Locate every uninfected red blood cell.
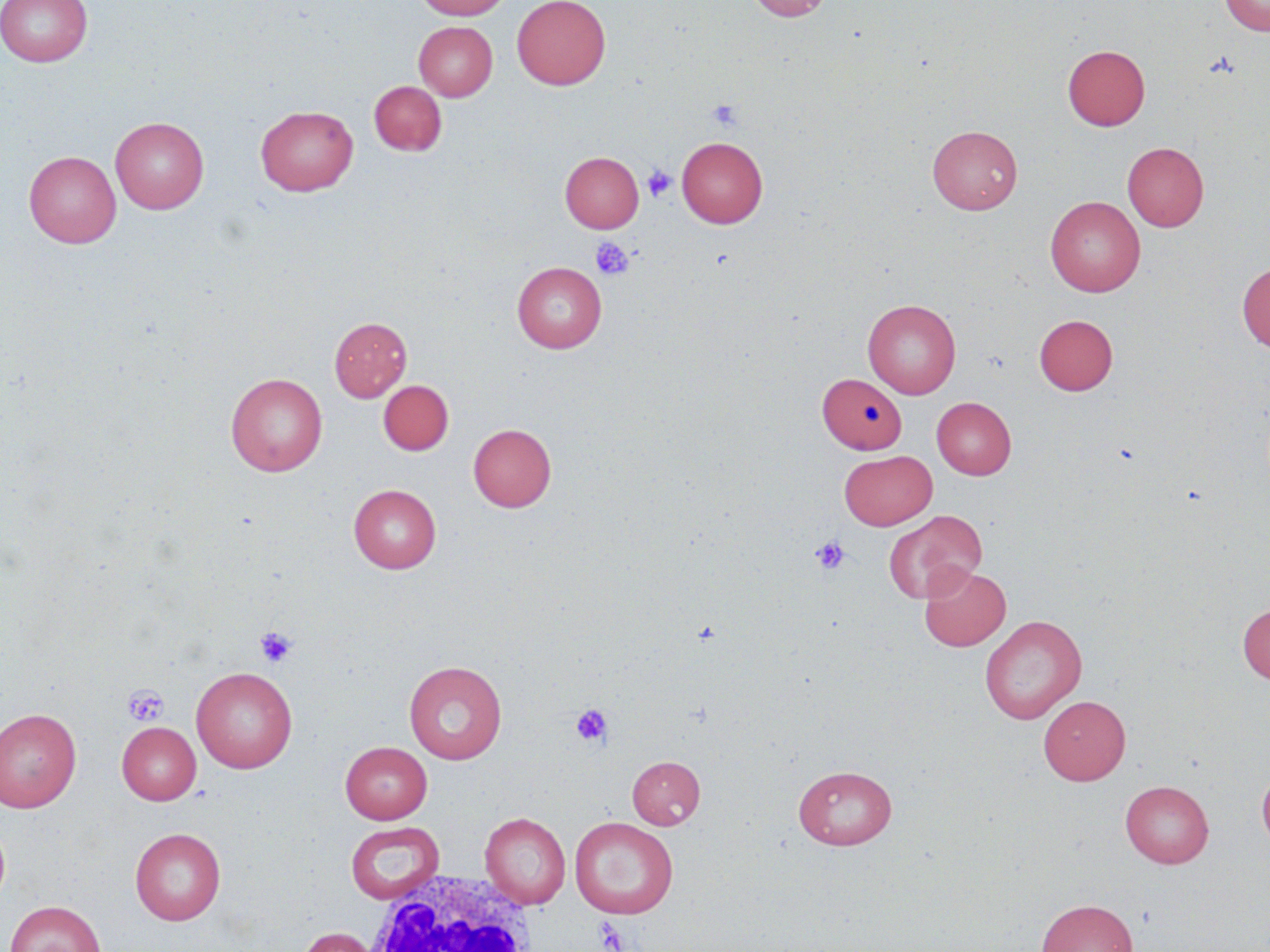

Approximate bounding boxes as [x1, y1, x2, y2] in pixels.
Uninfected red blood cells: [0, 0, 93, 66], [416, 0, 512, 19], [512, 0, 610, 90], [748, 0, 832, 21], [1219, 0, 1270, 36], [414, 21, 497, 101], [1063, 45, 1150, 130], [369, 80, 447, 156], [256, 105, 358, 196], [111, 116, 208, 213], [927, 125, 1022, 214], [677, 137, 767, 228], [1122, 142, 1208, 231], [24, 151, 121, 247], [560, 151, 644, 232], [1045, 196, 1145, 296], [512, 261, 606, 353], [1237, 262, 1270, 353], [863, 299, 961, 399], [1034, 314, 1118, 395], [330, 316, 412, 402], [818, 372, 906, 454], [226, 373, 328, 476], [378, 380, 454, 455], [932, 397, 1016, 479], [468, 423, 556, 512], [839, 450, 936, 530], [349, 484, 441, 573], [884, 509, 985, 603], [919, 564, 1011, 651], [1237, 603, 1270, 684], [980, 614, 1087, 723], [404, 661, 507, 764], [191, 666, 297, 773], [1039, 695, 1130, 785], [0, 708, 82, 812], [117, 722, 201, 804], [340, 741, 432, 824], [627, 755, 705, 829], [1257, 763, 1270, 851], [793, 764, 897, 849], [1121, 780, 1213, 868], [480, 812, 571, 908], [569, 817, 679, 919], [345, 821, 444, 904], [130, 827, 225, 925], [1036, 898, 1138, 952], [5, 899, 106, 952], [296, 926, 383, 952].

Summary:
  - White blood cell locations: [359, 870, 540, 952]
  - Platelet locations: [708, 99, 744, 130], [643, 165, 677, 202], [591, 237, 635, 281], [811, 536, 849, 575], [255, 626, 297, 667], [122, 685, 169, 727], [571, 705, 611, 746], [593, 917, 630, 951]
  - Slide-level diagnosis: negative for blood parasites
  - Modality: optical microscopy
  - Stain: May-Grünwald-Giemsa
  - Field of view: single
  - Preparation: thin blood film
  - Image size: 1270×952 pixels
  - Magnification: 1000x